Classify this cell by malaria status.
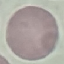
It is uninfected.

Summary:
  - Preparation: thin blood smear
  - Stain: Giemsa
  - Image type: automatically extracted cell patch, resized to 64 × 64 pixels
  - Capture: smartphone camera at the microscope eyepiece